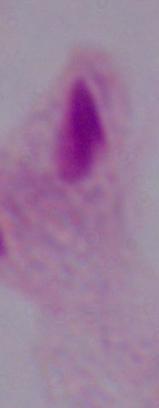
Captured at 1000x magnification. A trichomonad is shown. Micrograph.